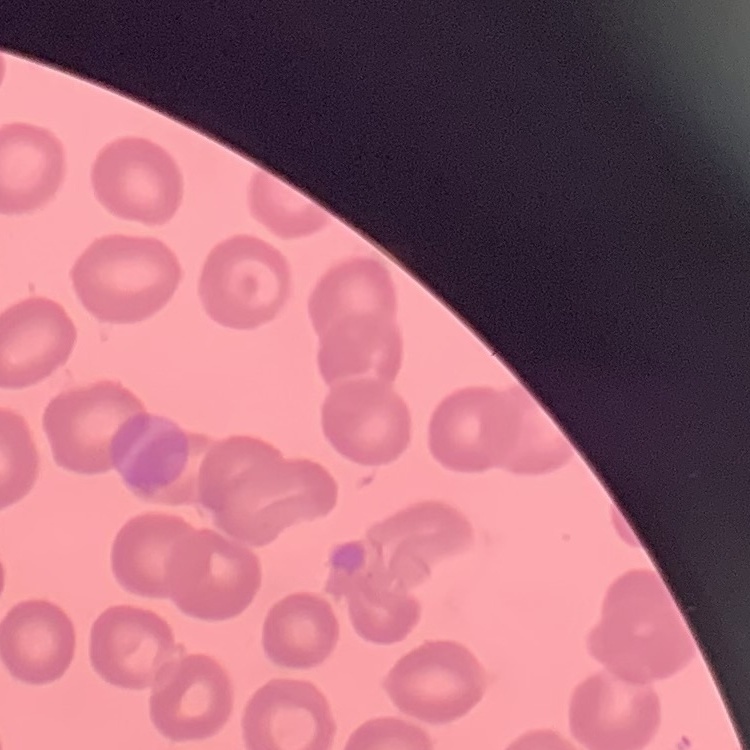
The erythrocytes show no rouleaux formation. One tile cut from a larger photomicrograph. Stained with either Field's or Giemsa. Thin peripheral smear.